Describe the morphology of the red blood cells.
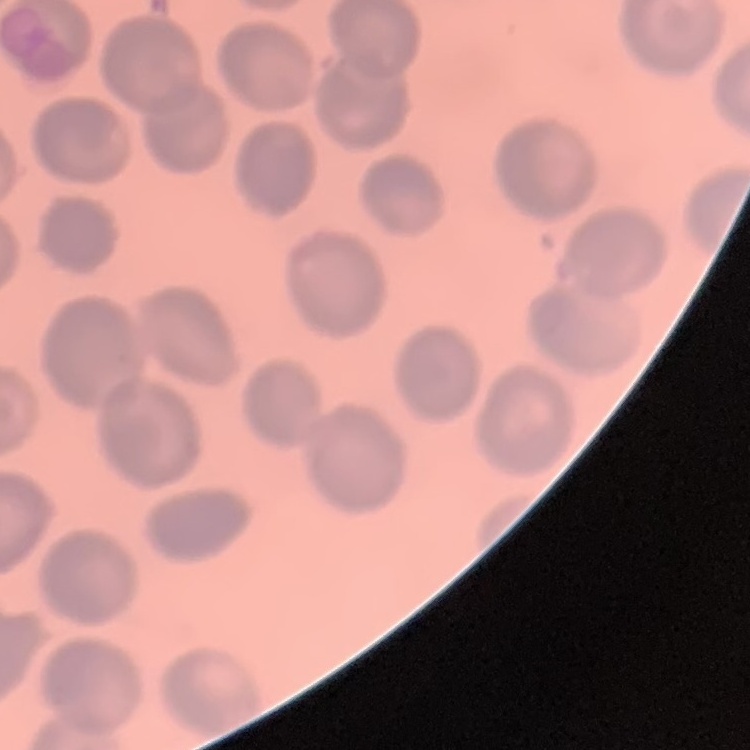
No rouleaux formation.

stain = Field's or Giemsa
preparation = thin blood film
image type = one tile cut from a larger photomicrograph